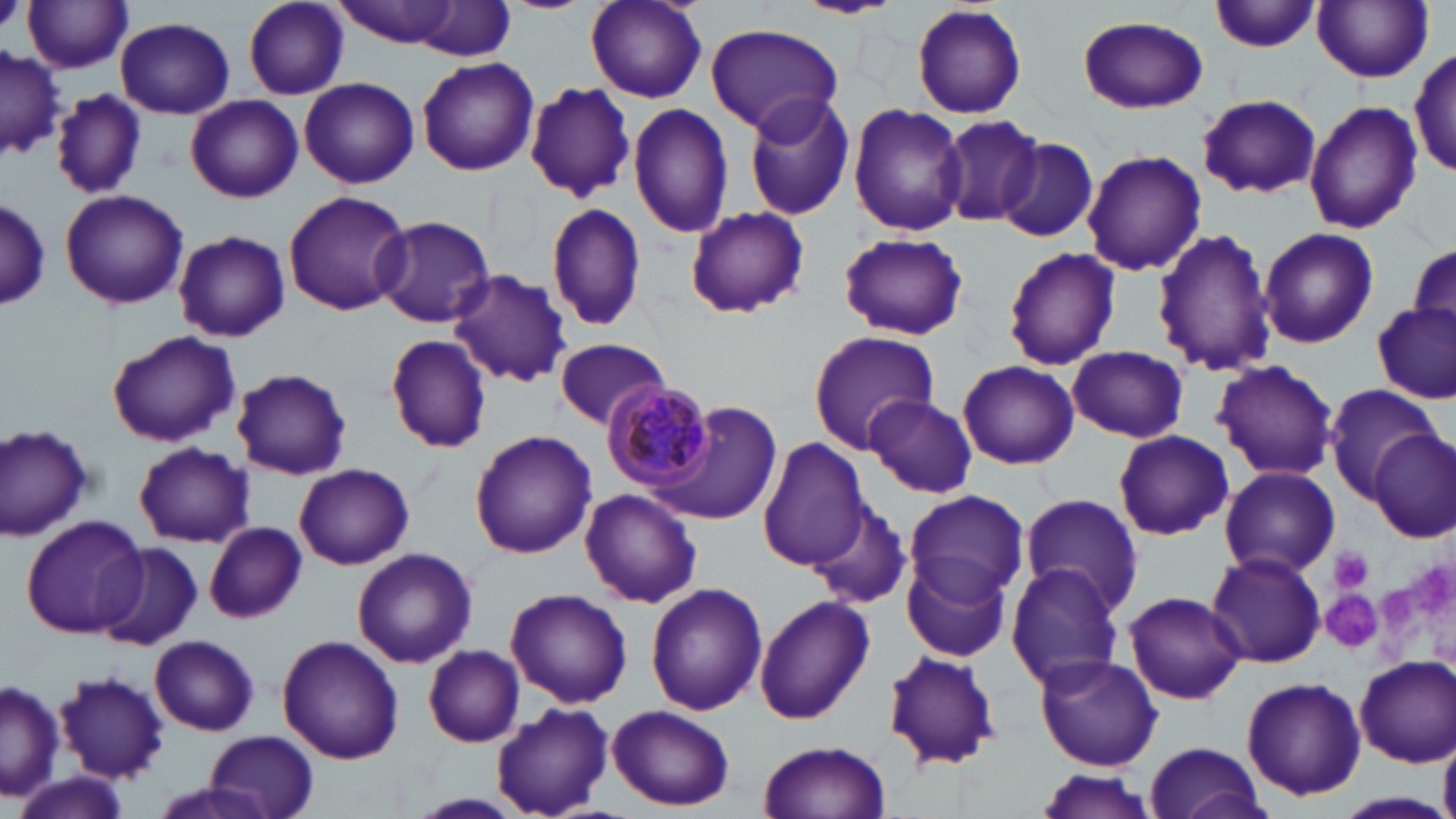 Approximate bounding boxes as [x1, y1, x2, y2] in pixels. Platelet locations: [1331, 547, 1372, 592], [1412, 561, 1453, 624], [1379, 582, 1414, 629], [1322, 587, 1384, 653]. Uninfected red blood cell locations: [794, 0, 902, 19], [23, 1, 134, 74], [242, 1, 350, 98], [330, 1, 467, 47], [586, 1, 706, 102], [1210, 1, 1321, 53], [1313, 1, 1433, 83], [411, 2, 515, 62], [912, 3, 1027, 120], [1076, 14, 1208, 113], [116, 17, 235, 118], [703, 22, 844, 135], [0, 47, 66, 160], [1411, 48, 1456, 175], [417, 58, 539, 177], [299, 77, 420, 188], [525, 82, 635, 202], [50, 88, 148, 199], [743, 92, 857, 221], [1198, 94, 1322, 198], [186, 96, 302, 202], [1304, 98, 1423, 235], [628, 101, 734, 239], [848, 101, 967, 237], [937, 112, 1046, 230], [994, 136, 1100, 242], [1082, 150, 1206, 277], [60, 190, 188, 310], [282, 190, 411, 318], [0, 198, 50, 312], [547, 202, 648, 333], [685, 207, 808, 318], [372, 215, 496, 327], [1257, 227, 1379, 349], [1150, 228, 1277, 378], [173, 230, 290, 342], [839, 231, 968, 341], [1408, 238, 1456, 336], [1000, 246, 1122, 371], [446, 269, 574, 389], [1373, 303, 1455, 402], [105, 329, 241, 446], [808, 331, 940, 452], [385, 333, 493, 453], [555, 338, 671, 429], [1067, 344, 1188, 443], [1211, 359, 1340, 481], [957, 360, 1079, 469], [232, 368, 353, 480], [1321, 382, 1442, 499], [863, 394, 978, 497], [658, 401, 782, 525], [1, 422, 95, 540], [1112, 429, 1234, 540], [1371, 429, 1453, 540], [470, 430, 597, 558], [758, 439, 870, 571], [133, 442, 254, 547], [294, 463, 414, 570], [1219, 466, 1340, 578], [579, 487, 702, 608], [905, 488, 1029, 606], [1020, 493, 1143, 614], [810, 504, 911, 610], [20, 514, 149, 640], [206, 522, 307, 623], [94, 543, 201, 650], [351, 548, 477, 667], [1206, 551, 1325, 667], [902, 552, 1012, 664], [1006, 564, 1127, 691], [645, 583, 767, 717], [505, 587, 632, 709], [1123, 591, 1248, 705], [752, 595, 875, 724], [276, 634, 405, 765], [151, 635, 259, 736], [423, 644, 525, 747], [881, 650, 1002, 773], [1035, 654, 1163, 770], [1354, 656, 1456, 766], [55, 670, 170, 782], [1242, 675, 1366, 802], [0, 679, 63, 803], [491, 703, 614, 817], [608, 704, 735, 811], [205, 729, 317, 818], [1439, 729, 1456, 819], [757, 739, 893, 819], [1141, 740, 1268, 819], [15, 769, 132, 819], [1032, 769, 1161, 817], [1335, 790, 1453, 819]. Plasmodium malariae-infected red blood cell locations: [602, 378, 717, 494]. Slide-level diagnosis: Plasmodium malariae. Captured at 1000x magnification. Optical microscopy. Thin blood smear. One field of a larger specimen. Image is 1456×819 pixels. May-Grünwald-Giemsa-stained preparation.